Outline each blood parasite and name the species.
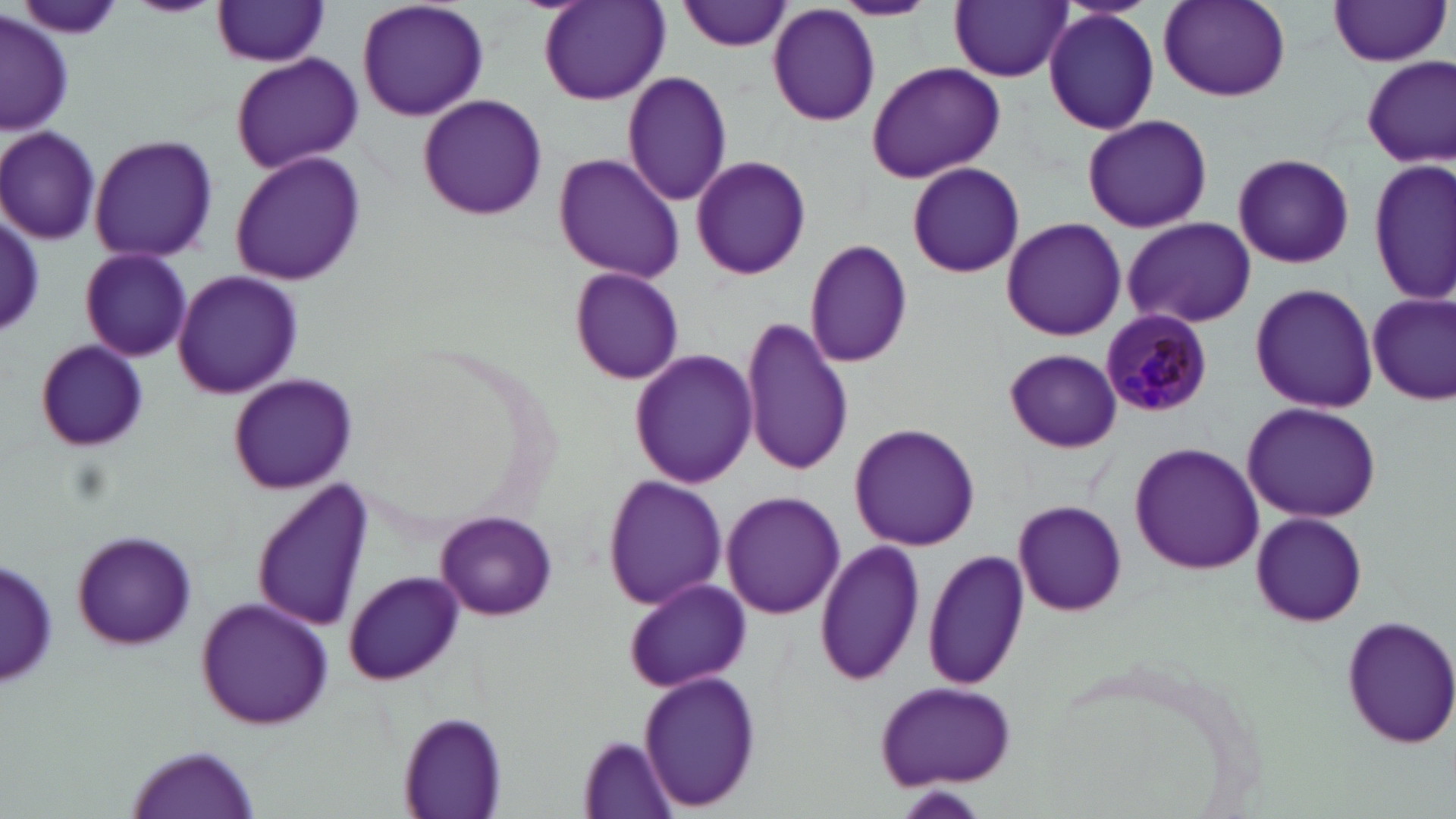
Approximate bounding boxes as (x1, y1, x2, y2) in pixels.
Plasmodium malariae-infected red blood cells: (1099, 309, 1210, 419).
No Plasmodium falciparum, Plasmodium ovale, Plasmodium vivax, Babesia divergens, or Trypanosoma brucei observed.

{
  "slide_level_diagnosis": "Plasmodium malariae",
  "preparation": "thin blood smear",
  "uninfected_red_blood_cell_locations": "approximate bounding boxes as (x1, y1, x2, y2) in pixels: (124, 0, 223, 17), (357, 0, 489, 123), (680, 0, 794, 52), (828, 0, 939, 21), (16, 1, 124, 43), (538, 1, 671, 106), (950, 1, 1071, 82), (1158, 1, 1290, 102), (1325, 1, 1452, 68), (209, 2, 333, 68), (767, 5, 881, 127), (1043, 7, 1160, 135), (2, 12, 76, 134), (230, 54, 363, 174), (1362, 56, 1455, 167), (865, 60, 1007, 183), (622, 70, 733, 207), (416, 93, 548, 222), (1082, 114, 1212, 233), (0, 126, 103, 243), (88, 134, 219, 262), (229, 149, 368, 287), (1231, 152, 1355, 268), (554, 153, 684, 283), (690, 154, 811, 281), (1371, 158, 1455, 305), (906, 161, 1025, 278), (2, 211, 46, 336), (1118, 216, 1257, 329), (1001, 217, 1128, 340), (804, 240, 913, 368), (78, 248, 192, 362), (568, 267, 686, 386), (171, 271, 303, 398), (1248, 282, 1379, 414), (1367, 292, 1454, 408), (742, 316, 853, 477), (33, 339, 153, 453), (629, 348, 758, 490), (1004, 348, 1123, 453), (228, 373, 358, 493), (1242, 401, 1383, 522), (850, 423, 981, 552), (1130, 442, 1262, 574), (603, 474, 729, 610), (252, 482, 374, 630), (721, 491, 844, 619), (1014, 501, 1127, 616), (1249, 510, 1368, 629), (437, 512, 556, 618), (69, 531, 200, 648), (815, 539, 926, 688), (922, 548, 1030, 691), (2, 552, 58, 691), (345, 572, 466, 684), (621, 577, 756, 694), (195, 597, 337, 728), (1341, 613, 1456, 751), (642, 672, 761, 810), (875, 682, 1019, 788), (398, 709, 509, 817), (581, 734, 679, 816), (132, 744, 255, 817), (893, 787, 992, 819)",
  "stain": "May-Grünwald-Giemsa",
  "field_of_view": "single",
  "modality": "optical microscopy",
  "magnification": "1000x",
  "image_size": "1456×819 pixels"
}